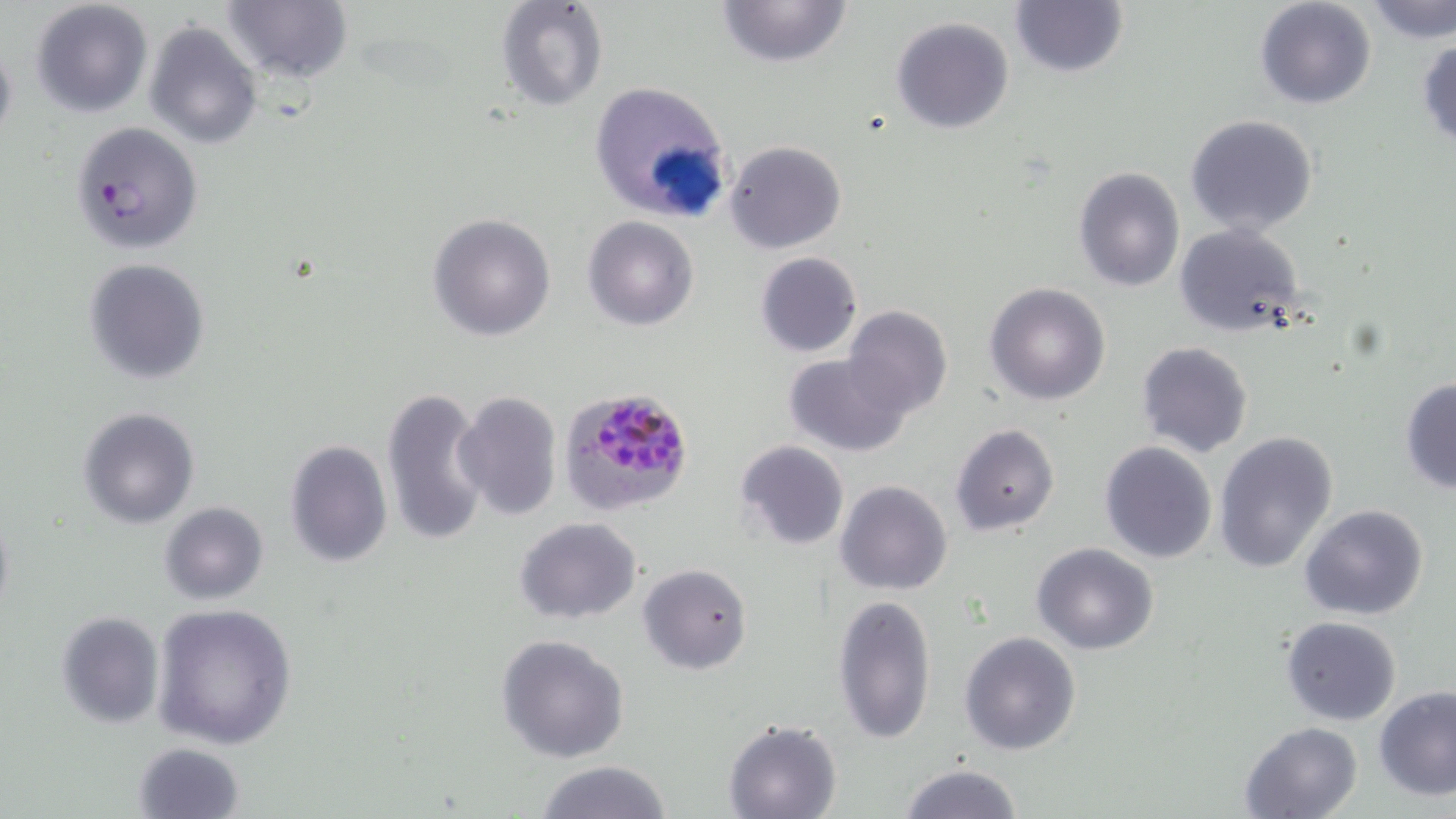

Summary:
  - Coordinate format: approximate bounding boxes as [x1, y1, x2, y2] in pixels
  - Uninfected red blood cell locations: [30, 0, 155, 118], [222, 0, 353, 86], [494, 0, 608, 111], [716, 0, 854, 68], [1254, 0, 1378, 110], [1363, 0, 1456, 44], [1008, 1, 1129, 80], [891, 16, 1015, 134], [145, 20, 262, 150], [1415, 37, 1456, 149], [0, 38, 18, 157], [587, 80, 735, 225], [1186, 115, 1319, 237], [68, 122, 202, 255], [725, 140, 846, 254], [1071, 165, 1187, 292], [428, 212, 556, 341], [583, 216, 698, 331], [1173, 222, 1308, 338], [755, 252, 862, 358], [82, 257, 211, 384], [984, 283, 1112, 405], [842, 305, 953, 421], [1135, 341, 1253, 459], [781, 352, 912, 457], [1399, 376, 1456, 493], [381, 386, 492, 548], [453, 390, 562, 520], [78, 407, 200, 529], [950, 423, 1060, 536], [1213, 431, 1340, 574], [284, 439, 392, 569], [735, 440, 849, 550], [1099, 441, 1218, 565], [835, 480, 953, 596], [159, 502, 269, 604], [1300, 503, 1430, 621], [514, 517, 642, 624], [1033, 542, 1160, 655], [638, 562, 752, 675], [832, 594, 936, 745], [151, 602, 299, 749], [56, 611, 165, 729], [1281, 616, 1401, 724], [958, 631, 1081, 755], [495, 633, 629, 762], [1374, 684, 1456, 799], [723, 720, 844, 818], [1240, 722, 1363, 817], [134, 740, 244, 818], [532, 760, 674, 819], [897, 763, 1023, 819]
  - Plasmodium falciparum-infected red blood cell locations: [559, 383, 695, 518]
  - Slide-level diagnosis: Plasmodium falciparum
  - Magnification: 1000x
  - Stain: May-Grünwald-Giemsa
  - Image size: 1456×819 pixels
  - Modality: optical microscopy
  - Field of view: single
  - Preparation: thin blood film